Report the malaria status of this cell.
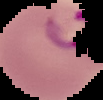

Parasitized.

Summary:
  - Image size: 103×100 pixels
  - Preparation: thin blood film
  - Image type: segmented cell region on a black background